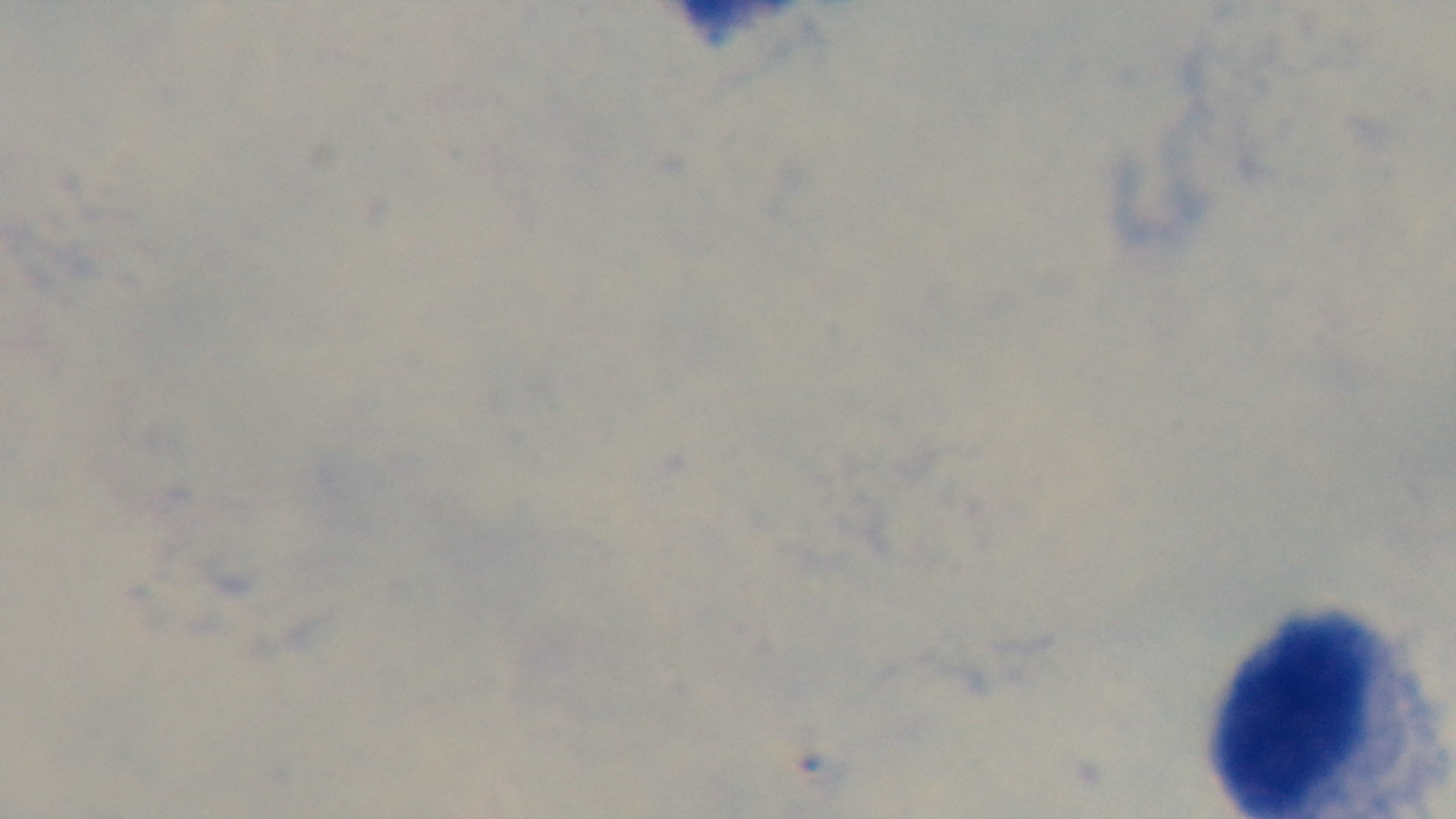
objective = 100x oil immersion
malaria status = uninfected
stain = Giemsa
modality = light microscopy
preparation = thick smear
capture = mounted 4K digital camera
field of view = one from the slide